State which cell type is depicted.
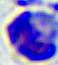
A leukocyte.

{
  "magnification": "400x",
  "modality": "micrograph"
}